Report the malaria status.
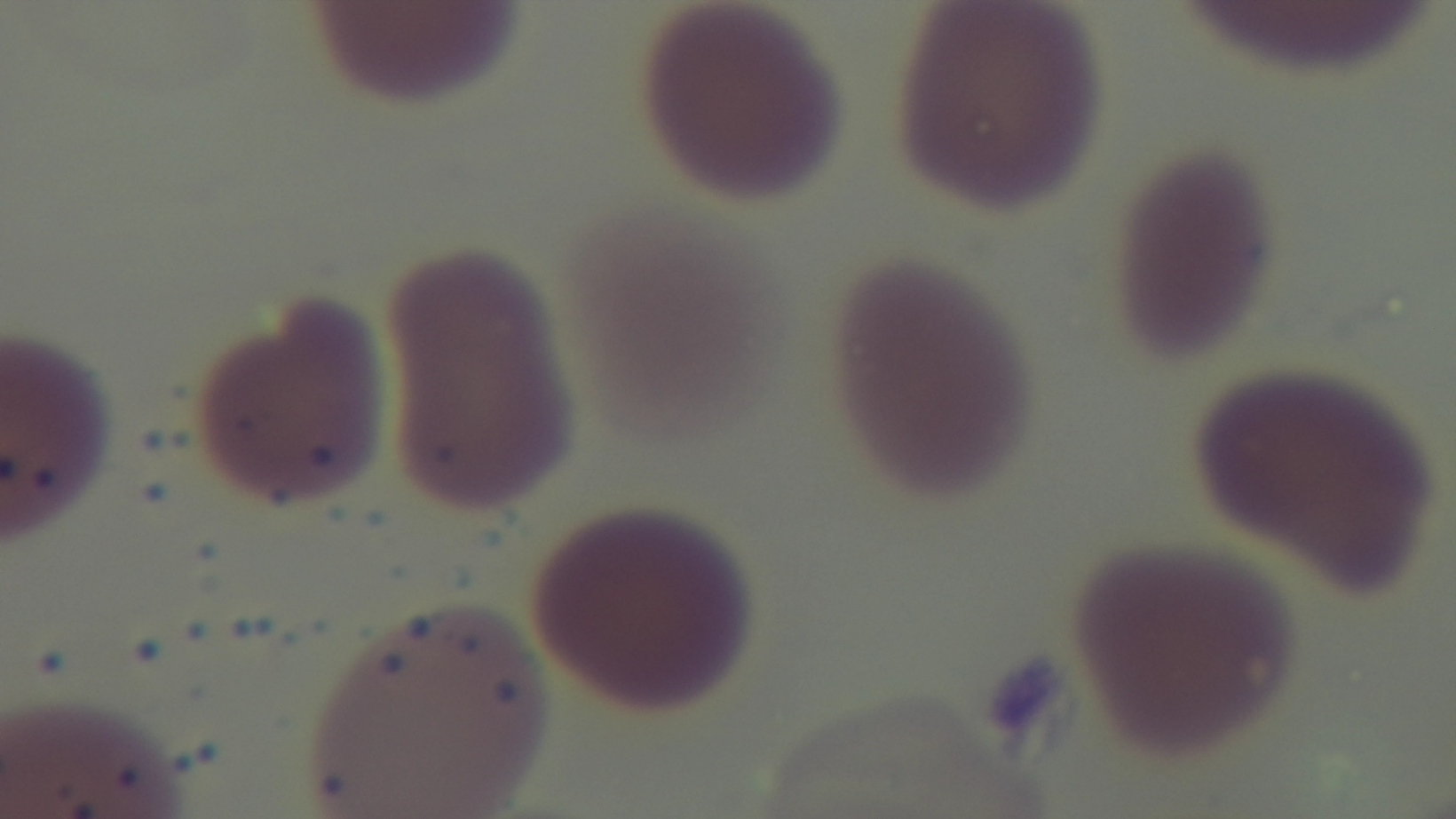

Uninfected.

Summary:
  - Objective: 100x oil immersion
  - Capture: mounted 4K digital camera
  - Stain: Giemsa
  - Modality: light microscopy
  - Field of view: one from the slide
  - Preparation: thin smear